State which parasite is depicted.
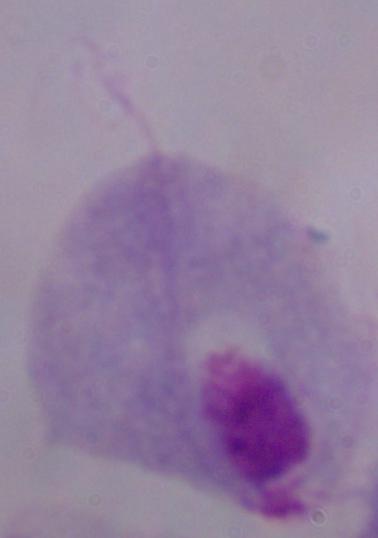

This is a trichomonad.

magnification: 1000x
modality: micrograph